Locate every blood parasite and identify its species.
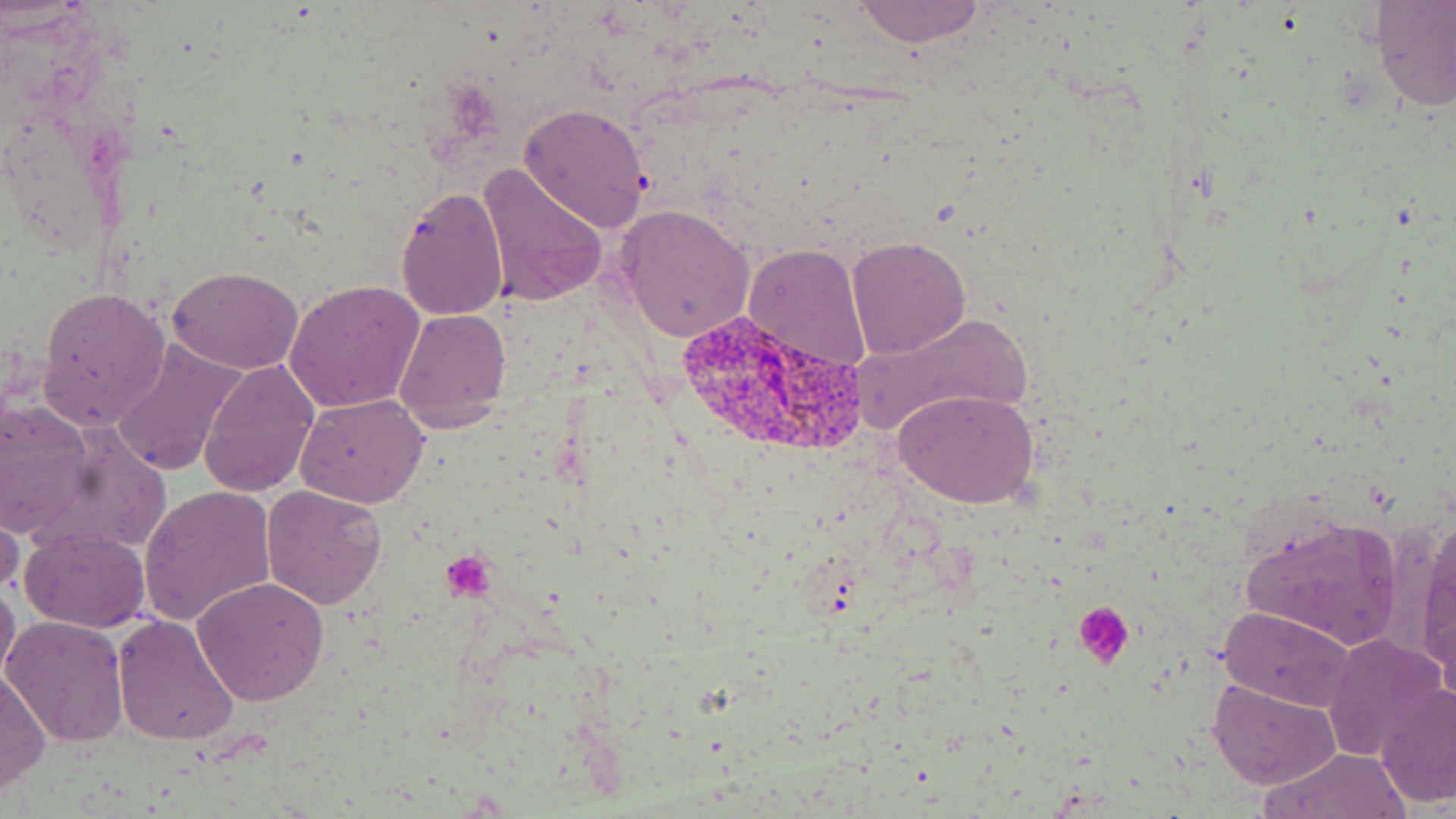
Approximate bounding boxes as [x1, y1, x2, y2] in pixels.
Plasmodium vivax-infected red blood cells: [678, 312, 863, 454].
No Plasmodium falciparum, Plasmodium ovale, Plasmodium malariae, Babesia divergens, or Trypanosoma brucei observed.

slide-level diagnosis = Plasmodium vivax
field of view = single
image size = 1456×819 pixels
platelet locations = approximate bounding boxes as [x1, y1, x2, y2] in pixels: [439, 552, 495, 602], [1073, 601, 1135, 667]
modality = optical microscopy
stain = May-Grünwald-Giemsa
uninfected red blood cell locations = approximate bounding boxes as [x1, y1, x2, y2] in pixels: [850, 0, 991, 48], [1368, 2, 1455, 112], [518, 102, 652, 233], [475, 163, 608, 308], [395, 185, 508, 322], [613, 203, 755, 342], [844, 236, 971, 358], [743, 242, 873, 377], [168, 265, 304, 375], [284, 279, 422, 414], [35, 287, 171, 431], [392, 308, 512, 431], [850, 310, 1031, 443], [109, 338, 244, 478], [199, 359, 319, 499], [893, 388, 1040, 510], [296, 393, 427, 507], [0, 397, 95, 543], [138, 484, 277, 627], [262, 484, 386, 611], [0, 491, 24, 604], [1236, 511, 1405, 653], [1414, 520, 1456, 685], [19, 528, 150, 632], [1, 573, 19, 692], [192, 577, 330, 706], [1217, 607, 1356, 711], [113, 613, 241, 744], [2, 614, 130, 746], [1322, 633, 1445, 760], [1, 667, 51, 796], [1209, 676, 1341, 789], [1376, 682, 1456, 807], [1260, 746, 1411, 818]
magnification = 1000x
preparation = thin blood smear